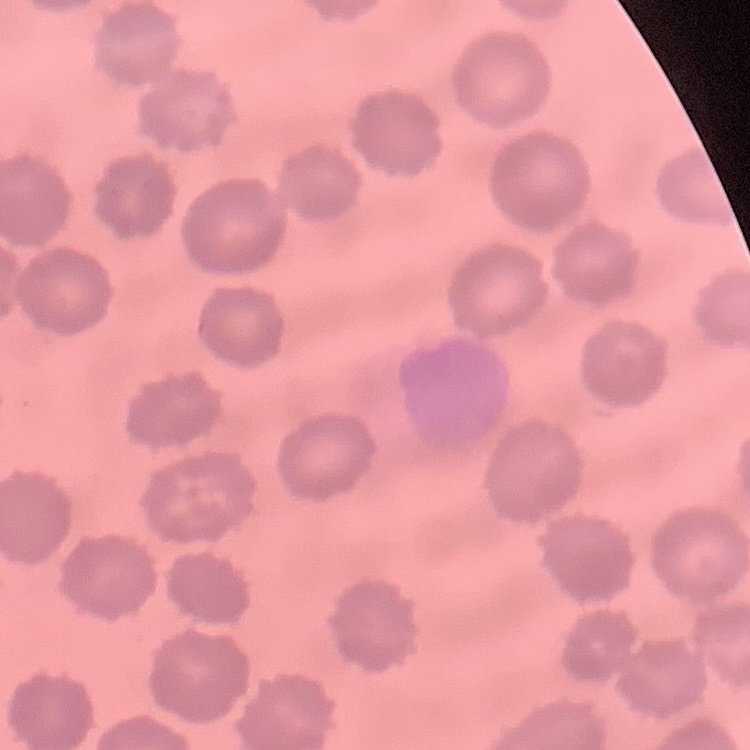
Summary:
  - Red blood cell morphology: no rouleaux formation
  - Preparation: thin blood film
  - Stain: Field's or Giemsa
  - Image type: square crop of a larger photomicrograph